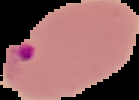
Summary:
  - Result: malaria parasites identified
  - Preparation: thin blood smear
  - Image size: 139×100 pixels
  - Image type: cell region segmented out of the field of view; surrounding area masked to black